Point out each leukocyte.
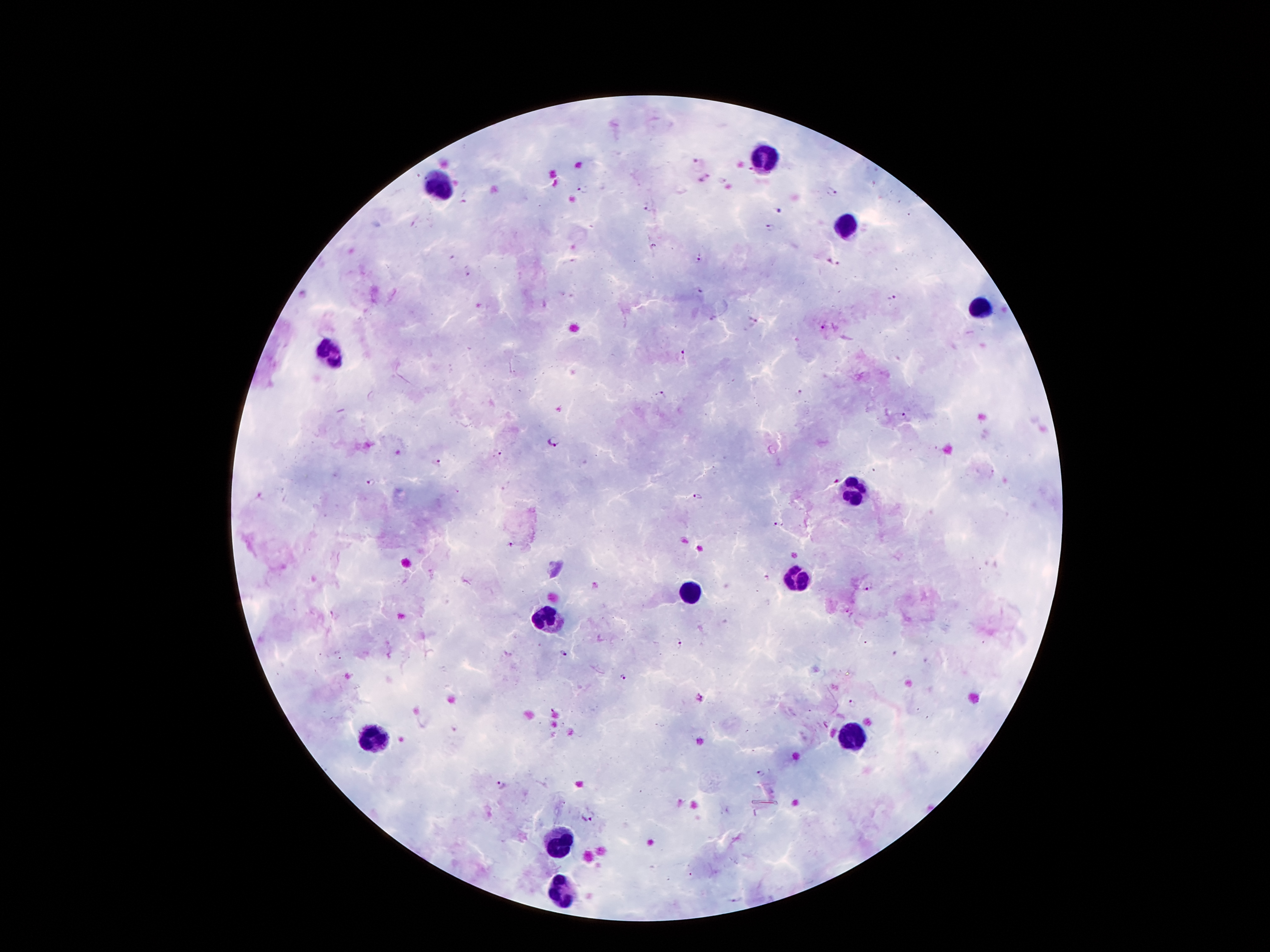

Approximate centers as (x, y) in pixels.
Leukocytes: (766, 159), (438, 184), (844, 228), (980, 306), (329, 352), (852, 493), (795, 574), (692, 591), (547, 621), (850, 736), (375, 738), (560, 839), (562, 891).

Malaria parasite locations: (698, 161), (705, 178), (722, 179), (581, 188), (832, 193), (648, 209), (779, 211), (769, 227), (699, 259), (833, 262), (467, 270), (698, 292), (891, 297), (752, 321), (822, 328), (684, 354), (660, 393), (903, 416), (553, 442), (497, 453), (437, 462), (370, 484), (697, 497), (778, 525), (511, 544), (867, 586), (334, 615), (678, 643), (563, 653), (622, 678), (699, 698), (852, 703), (455, 727), (760, 773), (502, 785), (587, 815). Smartphone photograph taken through the microscope eyepiece. Image is 1270×952 pixels. Giemsa-stained preparation. Patient malaria status: infected with Plasmodium falciparum. 100x magnification. Thick blood smear. One field from this slide.